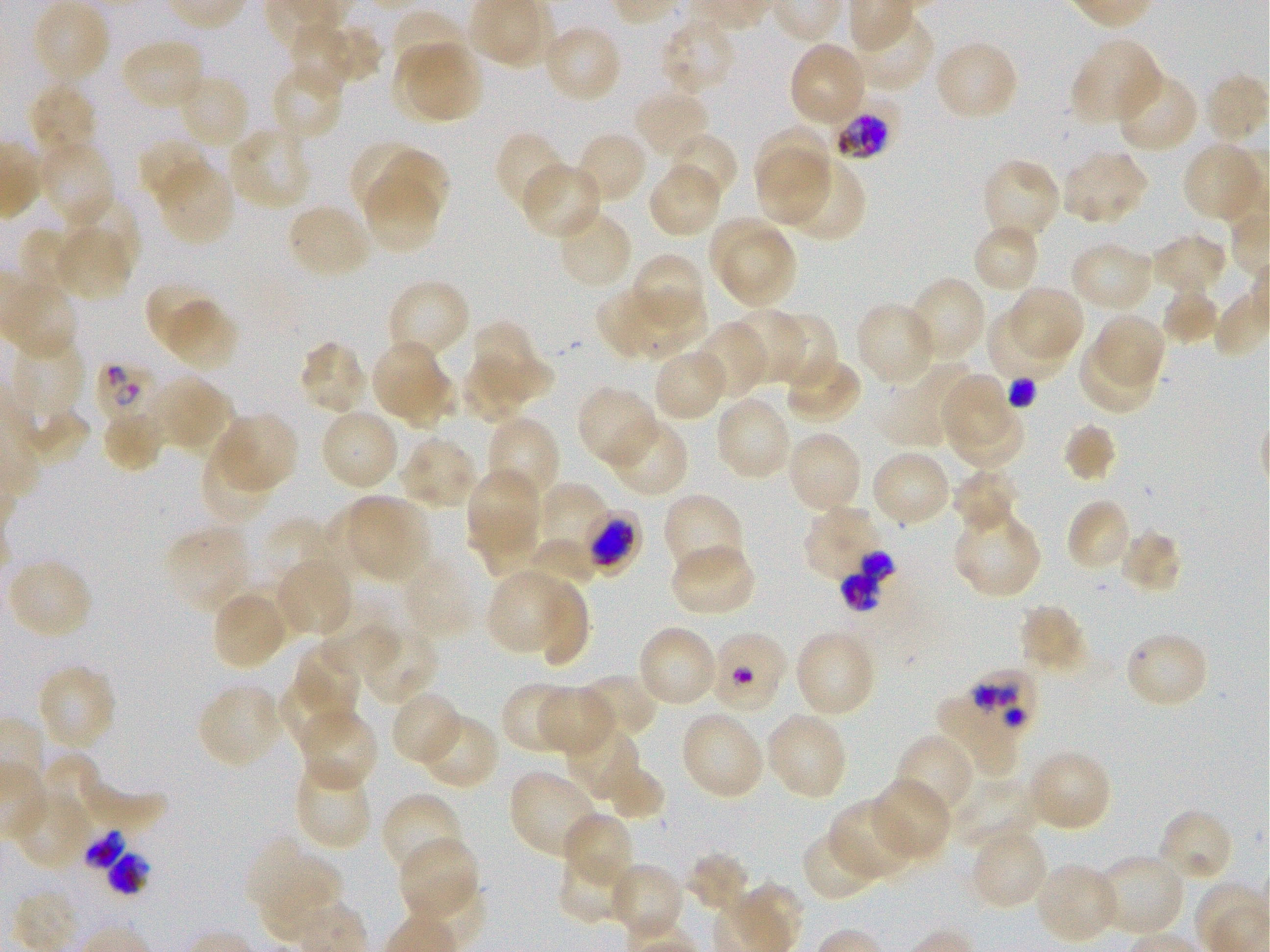
Approximate bounding rectangles given as corner coordinates in pixels from the top-left. Not every red blood cell is marked. A life-cycle stage — or a range of stages, where the recorded stages span more than one — follows each staged infected red blood cell. Locations of red blood cells of indeterminate infection status: (x1=583, y1=511, x2=644, y2=578), (x1=708, y1=629, x2=788, y2=714), (x1=930, y1=691, x2=1022, y2=773). Locations of infected red blood cells: (x1=830, y1=97, x2=899, y2=161) early trophozoite to early schizont; (x1=98, y1=361, x2=162, y2=426); (x1=839, y1=551, x2=899, y2=611); (x1=972, y1=665, x2=1039, y2=738); (x1=83, y1=830, x2=150, y2=895). Locations of uninfected red blood cells: (x1=31, y1=1, x2=110, y2=84), (x1=390, y1=10, x2=466, y2=84), (x1=849, y1=13, x2=935, y2=93), (x1=659, y1=15, x2=738, y2=95), (x1=288, y1=23, x2=360, y2=90), (x1=542, y1=23, x2=624, y2=104), (x1=318, y1=25, x2=382, y2=83), (x1=120, y1=37, x2=206, y2=111), (x1=934, y1=38, x2=1019, y2=122), (x1=1072, y1=38, x2=1164, y2=128), (x1=788, y1=42, x2=867, y2=128), (x1=407, y1=43, x2=480, y2=120), (x1=391, y1=47, x2=466, y2=119), (x1=269, y1=63, x2=346, y2=144), (x1=1115, y1=70, x2=1199, y2=154), (x1=178, y1=73, x2=250, y2=150), (x1=1205, y1=74, x2=1268, y2=142), (x1=27, y1=84, x2=99, y2=161), (x1=633, y1=89, x2=711, y2=160), (x1=227, y1=125, x2=312, y2=212), (x1=754, y1=125, x2=833, y2=205), (x1=494, y1=131, x2=568, y2=213), (x1=574, y1=131, x2=648, y2=206), (x1=666, y1=132, x2=739, y2=203), (x1=137, y1=136, x2=213, y2=205), (x1=37, y1=140, x2=116, y2=226), (x1=352, y1=141, x2=426, y2=213), (x1=1182, y1=142, x2=1265, y2=224), (x1=756, y1=148, x2=829, y2=225), (x1=379, y1=149, x2=448, y2=221), (x1=1060, y1=149, x2=1149, y2=226), (x1=981, y1=157, x2=1062, y2=242), (x1=782, y1=158, x2=867, y2=243), (x1=155, y1=159, x2=234, y2=245), (x1=521, y1=162, x2=602, y2=240), (x1=648, y1=163, x2=723, y2=238), (x1=363, y1=174, x2=440, y2=254), (x1=64, y1=193, x2=139, y2=274), (x1=286, y1=203, x2=370, y2=280), (x1=557, y1=209, x2=634, y2=291), (x1=709, y1=220, x2=783, y2=293), (x1=972, y1=222, x2=1041, y2=296), (x1=53, y1=227, x2=131, y2=301), (x1=20, y1=228, x2=81, y2=300), (x1=721, y1=229, x2=796, y2=310), (x1=1150, y1=232, x2=1228, y2=295), (x1=1069, y1=241, x2=1153, y2=313), (x1=630, y1=251, x2=707, y2=330), (x1=907, y1=276, x2=988, y2=361), (x1=386, y1=278, x2=471, y2=362), (x1=3, y1=280, x2=78, y2=361), (x1=144, y1=281, x2=216, y2=350), (x1=635, y1=286, x2=708, y2=357), (x1=1007, y1=286, x2=1085, y2=360), (x1=597, y1=289, x2=668, y2=358), (x1=1162, y1=289, x2=1219, y2=346), (x1=164, y1=300, x2=239, y2=372), (x1=855, y1=301, x2=939, y2=388), (x1=729, y1=308, x2=805, y2=384), (x1=985, y1=310, x2=1066, y2=384), (x1=772, y1=311, x2=837, y2=389), (x1=1093, y1=314, x2=1166, y2=390), (x1=471, y1=320, x2=554, y2=400), (x1=692, y1=321, x2=767, y2=400), (x1=12, y1=337, x2=86, y2=421), (x1=296, y1=340, x2=368, y2=414), (x1=371, y1=340, x2=447, y2=421), (x1=1079, y1=340, x2=1157, y2=414), (x1=653, y1=347, x2=729, y2=422), (x1=783, y1=355, x2=862, y2=426), (x1=461, y1=357, x2=530, y2=424), (x1=881, y1=362, x2=977, y2=446), (x1=394, y1=368, x2=457, y2=433), (x1=941, y1=373, x2=1016, y2=449), (x1=151, y1=376, x2=230, y2=452), (x1=576, y1=384, x2=659, y2=468), (x1=714, y1=396, x2=793, y2=482), (x1=946, y1=398, x2=1025, y2=469), (x1=24, y1=408, x2=90, y2=466), (x1=319, y1=408, x2=401, y2=492), (x1=101, y1=409, x2=164, y2=474), (x1=216, y1=411, x2=299, y2=492), (x1=485, y1=415, x2=562, y2=505), (x1=608, y1=416, x2=690, y2=498), (x1=1061, y1=421, x2=1118, y2=482), (x1=785, y1=429, x2=863, y2=514), (x1=400, y1=436, x2=478, y2=509), (x1=200, y1=441, x2=274, y2=525), (x1=871, y1=450, x2=952, y2=527), (x1=951, y1=468, x2=1020, y2=537), (x1=465, y1=469, x2=541, y2=555), (x1=537, y1=484, x2=612, y2=562), (x1=662, y1=491, x2=746, y2=579), (x1=347, y1=495, x2=429, y2=578), (x1=1066, y1=498, x2=1132, y2=574), (x1=325, y1=501, x2=395, y2=575), (x1=803, y1=506, x2=884, y2=583), (x1=466, y1=511, x2=542, y2=577), (x1=952, y1=511, x2=1043, y2=599), (x1=259, y1=518, x2=337, y2=591), (x1=164, y1=525, x2=251, y2=614), (x1=1118, y1=528, x2=1183, y2=595), (x1=528, y1=539, x2=596, y2=589), (x1=670, y1=544, x2=756, y2=617), (x1=402, y1=554, x2=478, y2=640), (x1=6, y1=558, x2=94, y2=641), (x1=275, y1=559, x2=352, y2=637), (x1=487, y1=569, x2=570, y2=655), (x1=240, y1=582, x2=312, y2=642), (x1=535, y1=582, x2=591, y2=670), (x1=212, y1=592, x2=288, y2=671), (x1=1017, y1=603, x2=1091, y2=674), (x1=319, y1=623, x2=397, y2=674), (x1=636, y1=624, x2=719, y2=708), (x1=360, y1=626, x2=440, y2=707), (x1=794, y1=628, x2=878, y2=717), (x1=1123, y1=631, x2=1210, y2=711), (x1=291, y1=644, x2=360, y2=718), (x1=36, y1=663, x2=117, y2=752), (x1=579, y1=673, x2=660, y2=741), (x1=278, y1=675, x2=352, y2=753), (x1=197, y1=682, x2=283, y2=769), (x1=500, y1=682, x2=576, y2=753), (x1=538, y1=686, x2=614, y2=755), (x1=391, y1=690, x2=463, y2=766), (x1=298, y1=708, x2=379, y2=793), (x1=679, y1=711, x2=765, y2=800), (x1=765, y1=711, x2=849, y2=800), (x1=421, y1=713, x2=500, y2=790), (x1=565, y1=725, x2=640, y2=802), (x1=895, y1=734, x2=975, y2=818), (x1=1026, y1=749, x2=1112, y2=832), (x1=43, y1=753, x2=103, y2=824), (x1=601, y1=758, x2=665, y2=821), (x1=294, y1=760, x2=372, y2=851), (x1=80, y1=763, x2=167, y2=829), (x1=509, y1=770, x2=599, y2=859), (x1=950, y1=775, x2=1036, y2=852), (x1=871, y1=779, x2=951, y2=862), (x1=11, y1=791, x2=93, y2=870), (x1=382, y1=793, x2=464, y2=878), (x1=828, y1=799, x2=916, y2=881), (x1=1156, y1=809, x2=1235, y2=885), (x1=562, y1=811, x2=634, y2=887), (x1=801, y1=829, x2=879, y2=903), (x1=969, y1=829, x2=1049, y2=911), (x1=245, y1=837, x2=344, y2=917), (x1=399, y1=838, x2=480, y2=921), (x1=556, y1=848, x2=633, y2=926), (x1=685, y1=850, x2=751, y2=913), (x1=1095, y1=853, x2=1186, y2=937), (x1=608, y1=861, x2=685, y2=941), (x1=1034, y1=862, x2=1120, y2=945). Giemsa-stained preparation. Image is 1270×952 pixels. Oil immersion, 100x objective (numerical aperture 1.25). Donor blood group O+. Thin blood smear. Static in-vitro culture of Plasmodium falciparum strain 3D7. Single field of view.